Assess this cell for malaria.
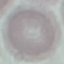
Uninfected.

Giemsa-stained preparation. Automatically extracted cell patch, resized to 64 × 64 pixels. Thin smear of blood. Acquired by smartphone through the microscope eyepiece.